Report the malaria status of this cell.
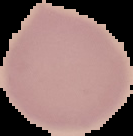

Uninfected.

image type = segmented cell region with the area outside set to black
preparation = thin blood film
image size = 133×136 pixels